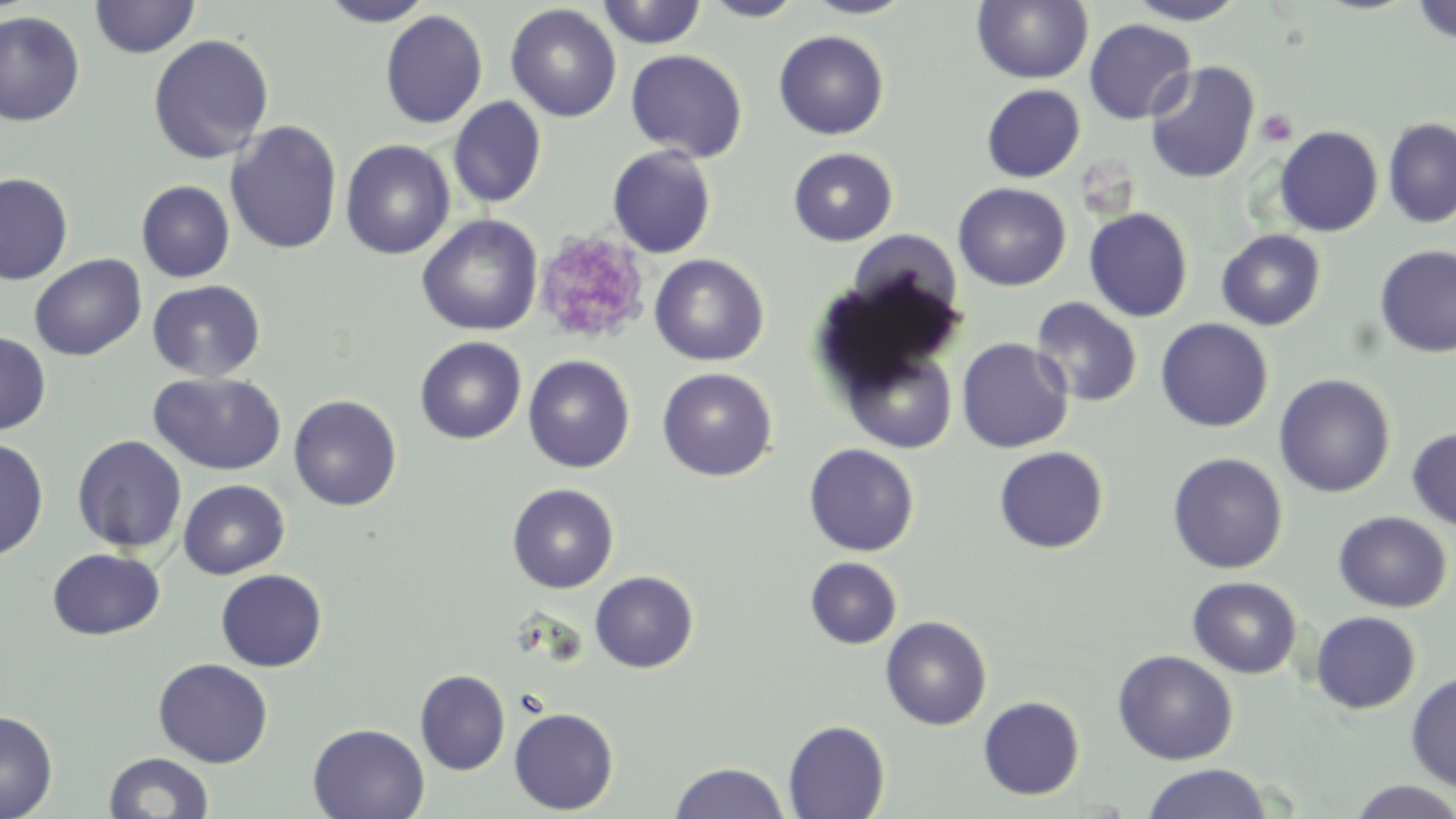 Approximate bounding boxes as [x1, y1, x2, y2] in pixels. Platelet locations: [1256, 109, 1298, 147], [533, 230, 650, 346]. Uninfected red blood cell locations: [89, 0, 200, 58], [319, 0, 435, 26], [596, 0, 708, 48], [802, 0, 918, 19], [972, 0, 1093, 84], [1126, 0, 1247, 25], [1412, 0, 1456, 45], [700, 1, 807, 22], [505, 3, 622, 122], [380, 10, 487, 129], [0, 11, 85, 127], [1084, 19, 1196, 124], [773, 30, 889, 140], [148, 34, 274, 164], [625, 49, 747, 163], [1144, 60, 1260, 184], [981, 84, 1085, 183], [448, 96, 546, 208], [1383, 118, 1456, 228], [225, 120, 343, 255], [1274, 126, 1382, 237], [340, 139, 455, 260], [607, 145, 717, 258], [788, 147, 898, 246], [0, 172, 73, 285], [136, 180, 235, 282], [144, 180, 247, 382], [953, 183, 1071, 291], [1084, 207, 1193, 322], [417, 215, 543, 336], [1216, 229, 1325, 330], [1375, 245, 1456, 357], [30, 253, 146, 361], [649, 253, 769, 366], [147, 280, 265, 382], [1031, 297, 1142, 407], [1155, 318, 1273, 432], [0, 331, 52, 435], [415, 336, 526, 444], [956, 337, 1074, 452], [843, 345, 959, 454], [523, 354, 635, 473], [657, 367, 777, 481], [148, 372, 286, 475], [1274, 373, 1395, 498], [288, 394, 401, 511], [1407, 427, 1456, 532], [72, 434, 188, 553], [0, 437, 49, 559], [804, 444, 919, 556], [994, 446, 1109, 553], [1167, 452, 1288, 574], [178, 479, 289, 579], [507, 483, 619, 593], [1333, 511, 1452, 612], [47, 548, 165, 640], [805, 557, 902, 649], [215, 569, 327, 672], [590, 571, 698, 673], [1188, 576, 1301, 678], [1310, 611, 1420, 714], [880, 615, 992, 730], [1113, 649, 1238, 765], [153, 658, 273, 768], [415, 669, 510, 775], [1405, 670, 1456, 793], [978, 696, 1085, 800], [509, 707, 618, 815], [0, 709, 58, 819], [783, 720, 890, 818], [307, 723, 430, 818], [105, 751, 214, 819], [670, 762, 790, 819], [1142, 763, 1273, 819], [1345, 780, 1456, 818]. Slide-level diagnosis: no evidence of blood parasites. Captured at 1000x magnification. One field of a larger specimen. Optical microscopy. May-Grünwald-Giemsa stain. Image is 1456×819 pixels. Thin blood film.